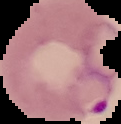
preparation: thin blood smear
image_size: 121×124 pixels
image_type: segmented cell region on a black background
result: Plasmodium parasites identified